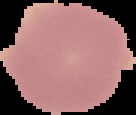
Summary:
  - Result: negative for malaria parasites
  - Preparation: thin blood film
  - Image size: 136×115 pixels
  - Image type: segmented cell region on a black background